Assess the morphology of the erythrocytes.
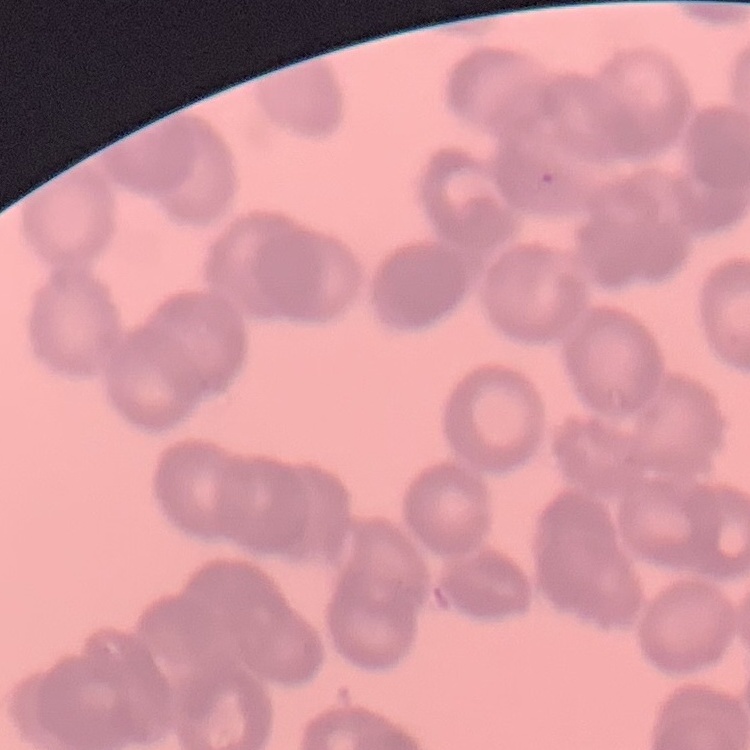
They show rouleaux formation.

Summary:
  - Image type: one tile cut from a larger photomicrograph
  - Preparation: thin blood smear
  - Stain: Field's or Giemsa